Locate every Plasmodium parasite.
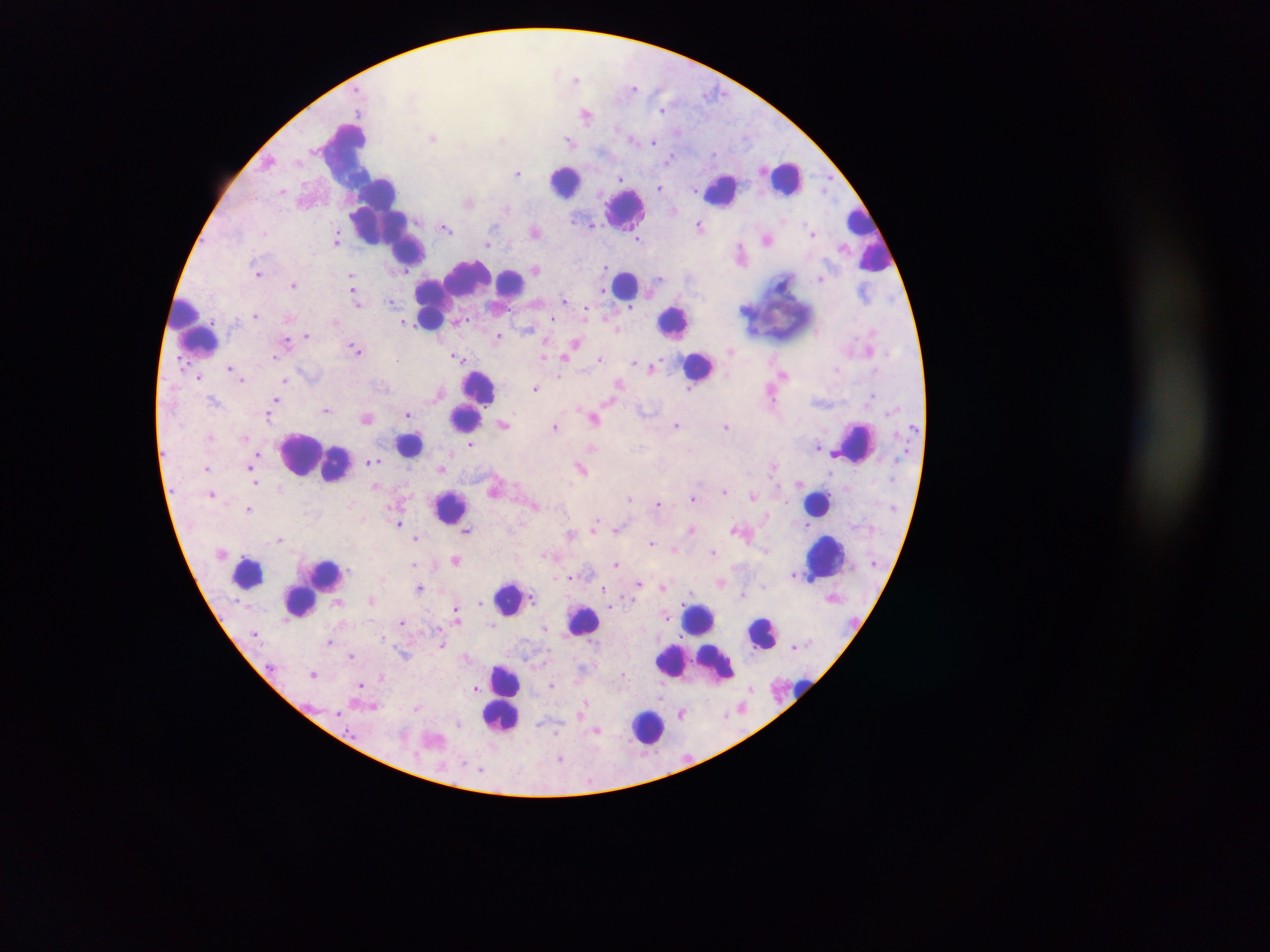
Approximate centers as {x, y} in pixels.
Plasmodium parasites: {576, 78}, {634, 87}, {663, 110}, {586, 115}, {432, 137}, {501, 138}, {654, 141}, {570, 142}, {461, 146}, {715, 154}, {669, 159}, {269, 162}, {517, 173}, {621, 177}, {660, 187}, {826, 187}, {282, 190}, {469, 202}, {507, 208}, {674, 210}, {592, 224}, {699, 225}, {446, 227}, {535, 231}, {265, 233}, {812, 233}, {639, 239}, {767, 239}, {337, 240}, {488, 243}, {740, 249}, {606, 267}, {536, 269}, {407, 271}, {257, 272}, {351, 277}, {659, 278}, {820, 279}, {293, 285}, {604, 290}, {354, 293}, {565, 299}, {391, 301}, {357, 302}, {630, 306}, {585, 312}, {256, 315}, {553, 318}, {405, 322}, {527, 329}, {617, 330}, {306, 335}, {499, 335}, {575, 344}, {356, 349}, {731, 351}, {544, 355}, {565, 356}, {274, 357}, {458, 357}, {600, 358}, {634, 361}, {653, 366}, {230, 368}, {783, 374}, {199, 378}, {242, 379}, {285, 379}, {619, 383}, {535, 388}, {690, 390}, {275, 400}, {213, 401}, {609, 402}, {326, 410}, {408, 415}, {269, 416}, {367, 418}, {595, 418}, {504, 423}, {677, 425}, {726, 426}, {554, 427}, {209, 437}, {470, 444}, {818, 445}, {592, 448}, {255, 455}, {373, 461}, {251, 465}, {775, 466}, {581, 467}, {442, 468}, {207, 469}, {255, 483}, {724, 490}, {213, 493}, {753, 496}, {629, 498}, {693, 498}, {658, 503}, {535, 505}, {249, 509}, {399, 523}, {595, 524}, {618, 528}, {691, 529}, {735, 529}, {467, 531}, {570, 535}, {280, 538}, {415, 538}, {651, 543}, {674, 549}, {714, 553}, {545, 555}, {457, 560}, {414, 565}, {617, 565}, {794, 574}, {570, 577}, {638, 582}, {663, 587}, {419, 588}, {604, 589}, {744, 594}, {370, 600}, {480, 603}, {610, 607}, {456, 613}, {667, 615}, {402, 620}, {493, 625}, {545, 628}, {382, 637}, {330, 642}, {442, 645}, {405, 654}, {351, 656}, {466, 657}, {313, 673}, {381, 677}, {552, 684}, {361, 685}, {476, 688}, {586, 703}, {374, 706}, {418, 707}, {339, 712}, {682, 713}, {459, 723}, {597, 730}, {557, 732}, {493, 745}, {561, 758}, {481, 769}.

field_of_view: single
preparation: thick blood film
capture: mobile-phone photograph through a microscope
country: Ghana
image_size: 1270×952 pixels
leukocyte_locations: 'approximate centers as {x, y} in pixels: {346, 153}, {786, 177}, {565, 181}, {720, 190}, {376, 193}, {627, 208}, {858, 218}, {377, 229}, {409, 249}, {877, 258}, {625, 282}, {453, 284}, {512, 284}, {775, 308}, {185, 311}, {430, 319}, {674, 321}, {201, 341}, {699, 367}, {479, 386}, {465, 419}, {855, 443}, {409, 444}, {308, 454}, {818, 502}, {451, 506}, {826, 556}, {247, 573}, {326, 573}, {313, 584}, {508, 599}, {300, 601}, {700, 619}, {583, 620}, {765, 633}, {694, 664}, {507, 680}, {800, 685}, {500, 717}, {647, 726}'